Give the extent of all uninfected red blood cells.
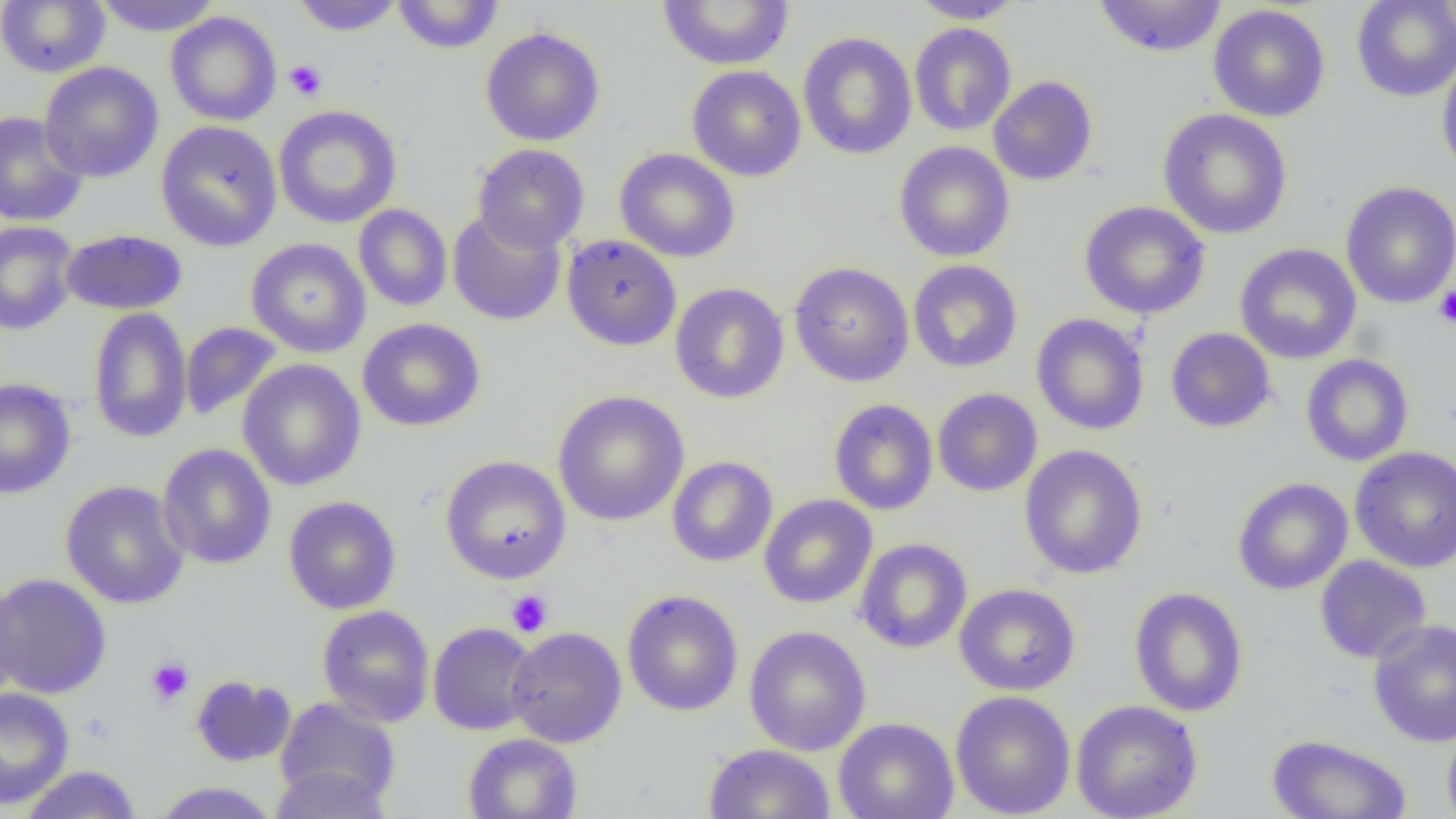
Approximate bounding boxes as named x1/y1/x2/y2 corners in pixels.
Uninfected red blood cells: (x1=92, y1=0, x2=223, y2=37), (x1=292, y1=0, x2=403, y2=36), (x1=392, y1=0, x2=505, y2=54), (x1=657, y1=0, x2=794, y2=70), (x1=908, y1=0, x2=1027, y2=23), (x1=1092, y1=0, x2=1228, y2=58), (x1=1351, y1=0, x2=1456, y2=102), (x1=0, y1=1, x2=110, y2=78), (x1=1208, y1=4, x2=1330, y2=122), (x1=165, y1=12, x2=281, y2=126), (x1=909, y1=23, x2=1016, y2=136), (x1=480, y1=27, x2=605, y2=146), (x1=797, y1=32, x2=917, y2=160), (x1=1436, y1=51, x2=1456, y2=181), (x1=39, y1=62, x2=163, y2=183), (x1=686, y1=65, x2=806, y2=182), (x1=988, y1=76, x2=1098, y2=186), (x1=273, y1=105, x2=402, y2=229), (x1=1158, y1=108, x2=1293, y2=240), (x1=0, y1=111, x2=88, y2=227), (x1=156, y1=120, x2=283, y2=252), (x1=894, y1=141, x2=1015, y2=262), (x1=472, y1=144, x2=590, y2=253), (x1=615, y1=147, x2=741, y2=263), (x1=1340, y1=181, x2=1456, y2=309), (x1=1079, y1=201, x2=1210, y2=319), (x1=353, y1=204, x2=453, y2=311), (x1=448, y1=210, x2=566, y2=326), (x1=0, y1=222, x2=80, y2=336), (x1=60, y1=229, x2=188, y2=315), (x1=562, y1=235, x2=681, y2=351), (x1=246, y1=238, x2=371, y2=358), (x1=1234, y1=243, x2=1362, y2=364), (x1=908, y1=259, x2=1023, y2=373), (x1=789, y1=262, x2=914, y2=387), (x1=670, y1=283, x2=789, y2=404), (x1=87, y1=307, x2=192, y2=444), (x1=1032, y1=313, x2=1149, y2=435), (x1=357, y1=318, x2=485, y2=432), (x1=180, y1=321, x2=283, y2=422), (x1=1165, y1=327, x2=1275, y2=433), (x1=1300, y1=354, x2=1414, y2=466), (x1=238, y1=359, x2=366, y2=491), (x1=0, y1=378, x2=75, y2=499), (x1=932, y1=388, x2=1042, y2=497), (x1=552, y1=390, x2=689, y2=526), (x1=828, y1=398, x2=938, y2=515), (x1=158, y1=443, x2=276, y2=570), (x1=1019, y1=445, x2=1147, y2=579), (x1=1350, y1=446, x2=1456, y2=573), (x1=440, y1=455, x2=571, y2=584), (x1=667, y1=456, x2=778, y2=567), (x1=1232, y1=477, x2=1353, y2=595), (x1=60, y1=481, x2=190, y2=609), (x1=758, y1=494, x2=877, y2=609), (x1=283, y1=496, x2=401, y2=614), (x1=855, y1=538, x2=972, y2=654), (x1=1315, y1=555, x2=1431, y2=664), (x1=0, y1=573, x2=111, y2=699), (x1=0, y1=582, x2=22, y2=708), (x1=954, y1=583, x2=1080, y2=696), (x1=1129, y1=587, x2=1248, y2=717), (x1=622, y1=589, x2=744, y2=716), (x1=316, y1=605, x2=435, y2=727), (x1=1368, y1=619, x2=1456, y2=747), (x1=427, y1=622, x2=539, y2=736), (x1=505, y1=626, x2=627, y2=747), (x1=744, y1=626, x2=871, y2=756), (x1=191, y1=675, x2=296, y2=766), (x1=0, y1=687, x2=74, y2=809), (x1=950, y1=690, x2=1076, y2=818), (x1=275, y1=696, x2=400, y2=811), (x1=1071, y1=699, x2=1203, y2=819), (x1=833, y1=717, x2=959, y2=819), (x1=1442, y1=720, x2=1456, y2=819), (x1=463, y1=733, x2=582, y2=819), (x1=1266, y1=734, x2=1412, y2=819), (x1=703, y1=743, x2=835, y2=819), (x1=269, y1=764, x2=394, y2=819), (x1=19, y1=765, x2=142, y2=819), (x1=152, y1=782, x2=280, y2=818).

Summary:
  - Platelet locations: (x1=284, y1=60, x2=327, y2=101), (x1=1433, y1=285, x2=1456, y2=328), (x1=506, y1=590, x2=553, y2=637), (x1=146, y1=657, x2=194, y2=707)
  - Slide-level diagnosis: negative for blood parasites
  - Modality: optical microscopy
  - Image size: 1456×819 pixels
  - Preparation: thin blood smear
  - Field of view: one of a larger specimen
  - Magnification: 1000x